Locate and identify every blood parasite.
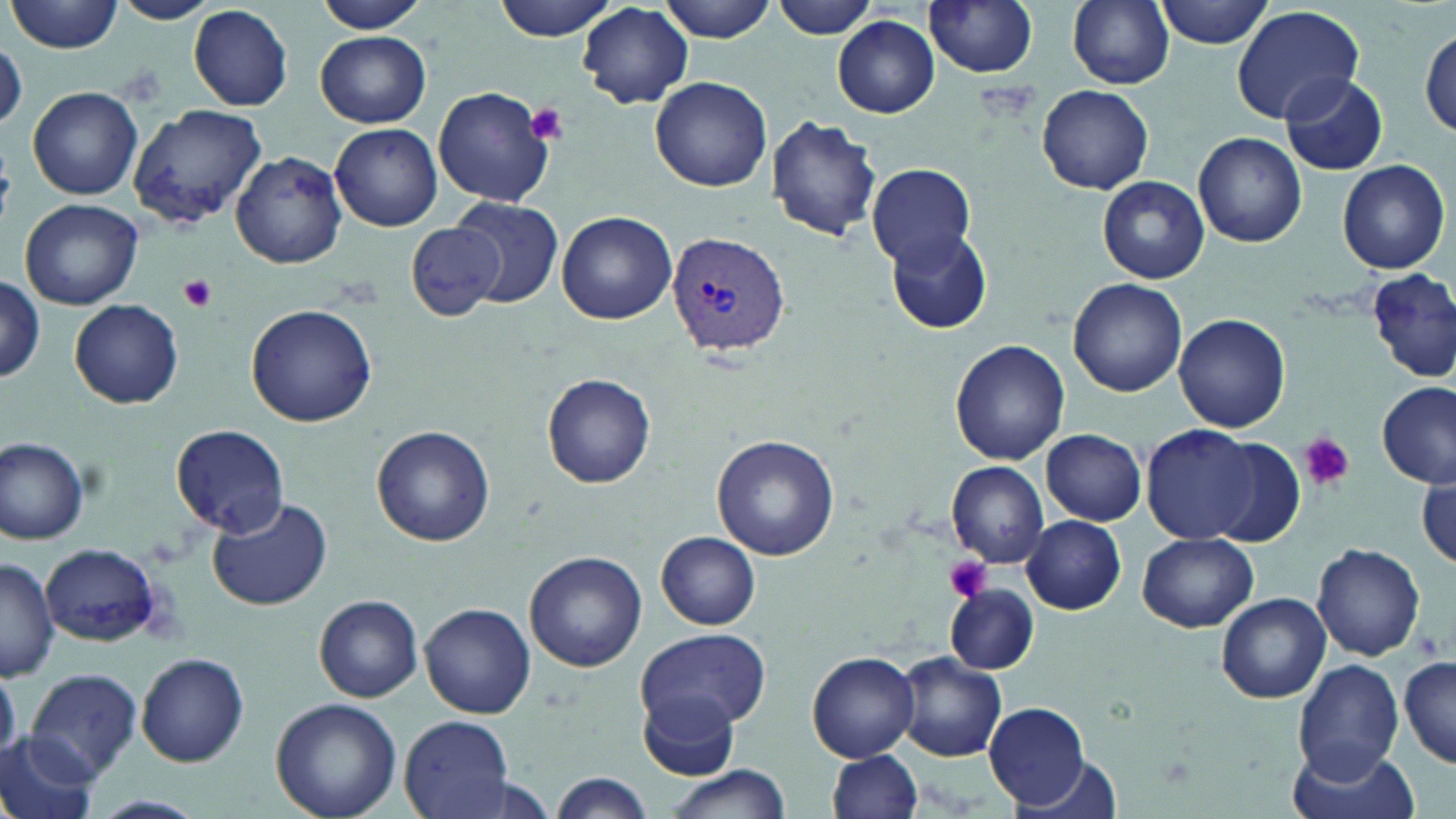

Approximate bounding boxes as (x1, y1, x2, y2) in pixels.
Plasmodium vivax-infected red blood cells: (665, 230, 790, 355).
No Plasmodium falciparum, Plasmodium ovale, Plasmodium malariae, Babesia divergens, or Trypanosoma brucei observed.

Platelet locations: (526, 104, 570, 145), (178, 275, 215, 312), (1298, 433, 1354, 490), (943, 555, 994, 603). Uninfected red blood cell locations: (10, 0, 122, 54), (113, 0, 215, 24), (317, 0, 433, 35), (493, 0, 623, 40), (659, 0, 777, 41), (769, 0, 882, 39), (924, 0, 1039, 78), (1067, 0, 1175, 88), (1154, 0, 1277, 48), (577, 4, 694, 108), (189, 5, 293, 111), (1232, 5, 1364, 125), (833, 16, 940, 118), (1419, 28, 1454, 142), (315, 31, 432, 128), (1, 39, 26, 132), (1279, 72, 1390, 176), (650, 75, 772, 192), (433, 86, 558, 207), (1036, 86, 1154, 195), (27, 87, 143, 201), (127, 104, 268, 226), (766, 114, 883, 244), (330, 123, 442, 231), (1192, 133, 1307, 247), (232, 150, 348, 268), (1337, 159, 1450, 274), (866, 161, 976, 268), (1098, 175, 1208, 284), (450, 195, 564, 308), (20, 198, 142, 310), (556, 209, 677, 324), (408, 220, 510, 322), (886, 228, 993, 333), (1365, 268, 1454, 383), (0, 275, 45, 382), (1069, 279, 1187, 396), (70, 298, 184, 409), (246, 303, 377, 428), (1172, 314, 1291, 433), (949, 338, 1070, 465), (542, 372, 657, 489), (1377, 382, 1454, 487), (171, 424, 291, 537), (372, 424, 495, 546), (1140, 424, 1265, 542), (1041, 428, 1147, 526), (711, 434, 839, 559), (1, 437, 92, 545), (1192, 438, 1307, 547), (946, 461, 1049, 565), (1418, 472, 1455, 573), (205, 498, 333, 613), (1021, 515, 1126, 614), (655, 530, 761, 629), (1136, 532, 1257, 632), (1312, 542, 1427, 661), (43, 545, 160, 645), (524, 550, 648, 672), (0, 557, 58, 681), (945, 585, 1038, 673), (1216, 593, 1331, 703), (314, 595, 423, 703), (420, 603, 536, 718), (636, 628, 768, 734), (807, 651, 921, 761), (134, 653, 249, 765), (893, 653, 1008, 763), (1398, 656, 1456, 767), (1294, 659, 1405, 782), (26, 668, 142, 780), (639, 694, 742, 777), (271, 699, 403, 819), (983, 702, 1095, 810), (399, 716, 514, 819), (0, 732, 100, 819), (1288, 742, 1417, 819), (825, 751, 924, 819), (1008, 756, 1127, 819), (660, 765, 792, 819), (547, 772, 655, 818), (90, 794, 205, 819). Slide-level diagnosis: Plasmodium vivax. Light microscopy. Thin blood smear. Image is 1456×819 pixels. May-Grünwald-Giemsa-stained preparation. 1000x magnification. Single field of view.